Assess this cell for malaria.
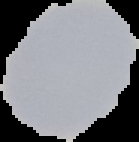
Uninfected.

From a thin blood film. Image is 139×142 pixels. Cell region segmented out of the field of view; the surrounding area is masked to black.